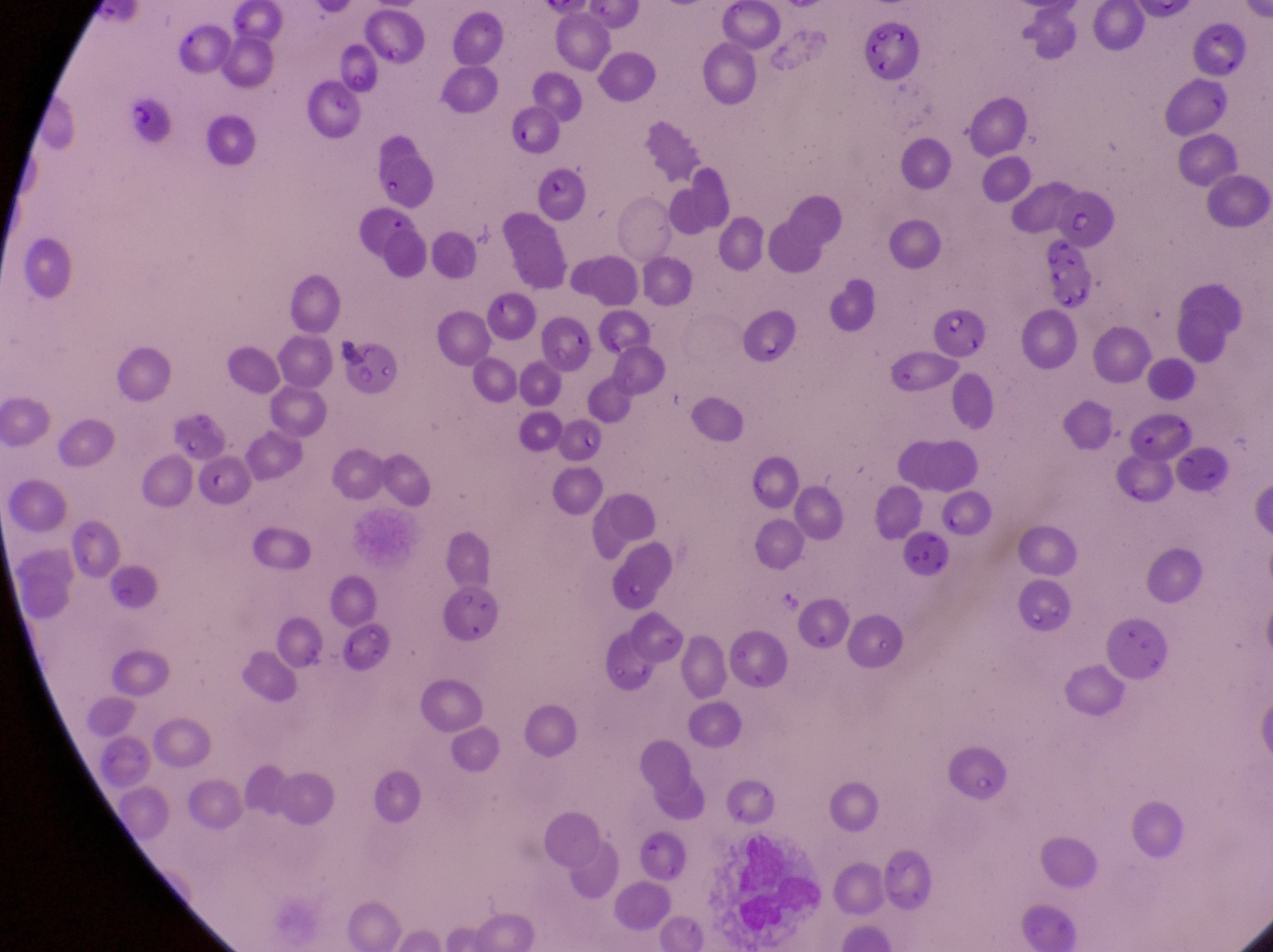
{
  "capture": "smartphone photograph through the eyepiece of an Olympus CX-23 microscope",
  "magnification": "1000x",
  "parasitised_red_blood_cell_locations": "approximate bounding boxes as (left, top, right, bottom) in pixels: (122, 93, 175, 146), (502, 107, 562, 157), (539, 160, 596, 227), (934, 304, 989, 361)",
  "artifact_platelet_like_body_stain_precipitate_or_debris_locations": "approximate bounding boxes as (left, top, right, bottom) in pixels: (1041, 235, 1098, 303)",
  "preparation": "thin blood smear",
  "image_size": "1273×952 pixels",
  "field_of_view": "single",
  "country": "Uganda"
}